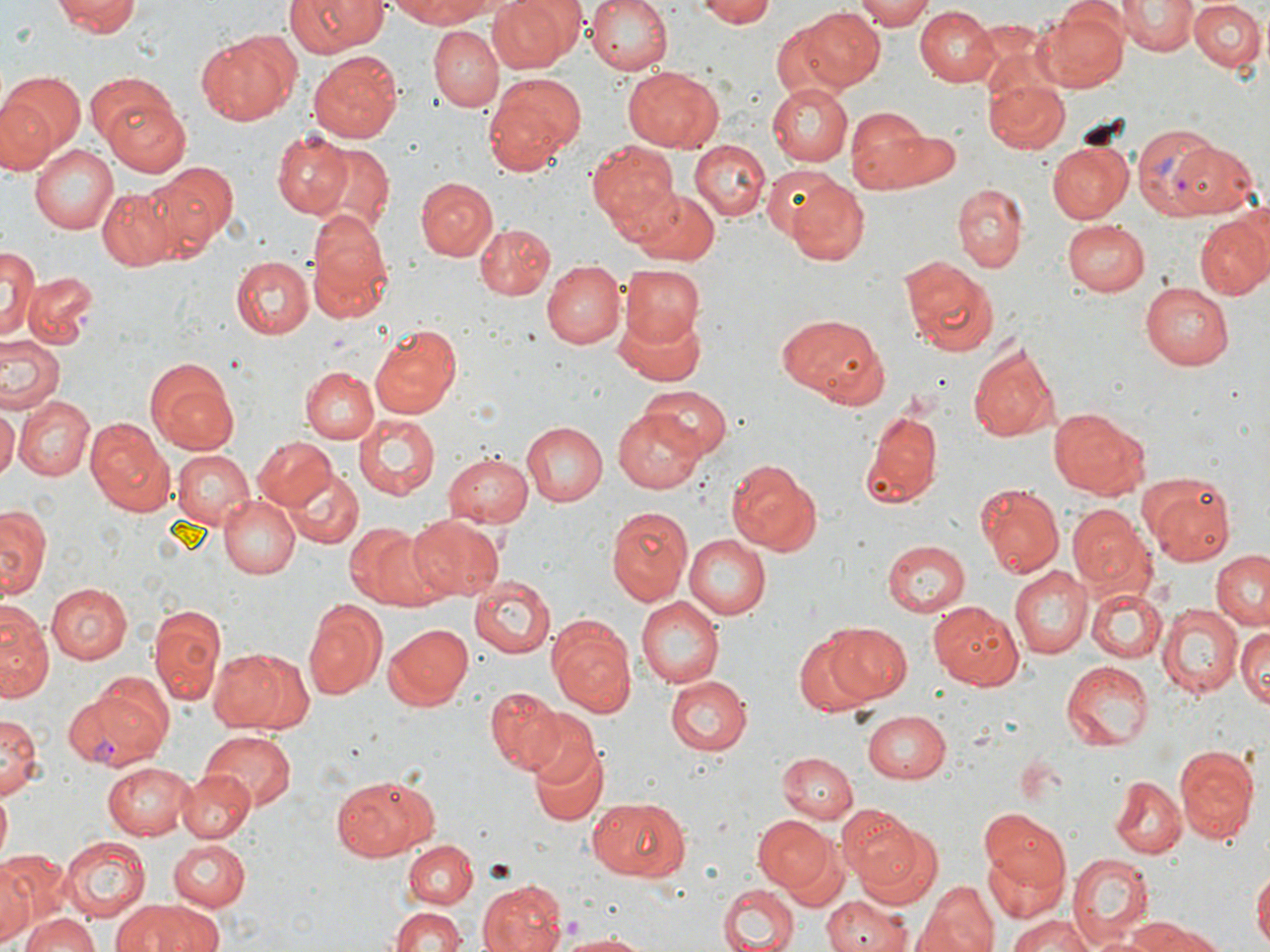
Summary:
  - Coordinate format: approximate bounding boxes as (x1,y1)-(x2,y2) corner pairs in pixels
  - Plasmodium vivax-infected red blood cell locations: (1130,124)-(1223,218), (66,679)-(171,768)
  - Uninfected red blood cell locations: (50,0)-(141,38), (284,0)-(389,58), (583,0)-(673,75), (855,0)-(938,29), (1119,0)-(1194,55), (387,1)-(497,28), (488,1)-(571,72), (697,1)-(780,27), (1190,1)-(1267,74), (1041,5)-(1130,89), (915,6)-(1001,85), (800,8)-(884,91), (769,21)-(849,99), (428,26)-(504,110), (194,30)-(300,126), (308,51)-(404,143), (623,66)-(723,152), (2,70)-(85,160), (482,73)-(585,175), (984,76)-(1070,156), (768,84)-(852,166), (97,86)-(191,173), (0,95)-(57,173), (845,106)-(932,192), (875,123)-(961,189), (270,128)-(352,217), (691,139)-(771,223), (585,140)-(679,228), (1048,141)-(1134,223), (28,142)-(118,235), (316,142)-(394,234), (1168,144)-(1259,217), (148,163)-(238,251), (761,164)-(841,241), (415,177)-(498,261), (785,178)-(869,265), (96,184)-(185,271), (954,185)-(1027,271), (630,189)-(720,265), (306,212)-(396,323), (1194,214)-(1269,299), (1061,219)-(1151,297), (474,223)-(557,299), (1,247)-(40,337), (231,255)-(314,340), (900,257)-(999,359), (543,261)-(624,349), (618,264)-(706,350), (23,270)-(99,348), (1141,280)-(1234,371), (611,306)-(710,387), (778,311)-(886,406), (369,324)-(461,418), (0,335)-(66,415), (968,339)-(1059,443), (300,365)-(379,443), (148,366)-(240,455), (639,385)-(732,458), (13,396)-(95,481), (0,404)-(18,481), (614,407)-(705,491), (1049,407)-(1150,499), (355,412)-(443,497), (860,412)-(942,511), (520,421)-(606,506), (87,425)-(176,517), (253,436)-(336,511), (170,449)-(255,530), (443,450)-(532,529), (725,461)-(822,554), (289,470)-(363,547), (1139,475)-(1239,565), (977,486)-(1064,579), (217,494)-(300,579), (0,504)-(49,601), (606,505)-(694,604), (1066,505)-(1155,594), (408,515)-(505,600), (344,525)-(429,608), (681,533)-(770,623), (881,540)-(971,615), (1210,550)-(1269,631), (1011,567)-(1090,658), (468,577)-(556,658), (48,584)-(132,665), (1085,588)-(1166,664), (636,597)-(724,688), (303,598)-(386,701), (930,600)-(1026,689), (1,603)-(52,702), (1158,603)-(1242,695), (149,604)-(226,706), (819,616)-(1009,699), (548,620)-(636,717), (1235,620)-(1270,710), (822,622)-(913,703), (385,624)-(473,710), (795,634)-(871,716), (209,645)-(308,734), (1062,660)-(1155,752), (664,676)-(749,754), (485,688)-(567,774), (863,710)-(953,784), (526,711)-(603,792), (0,714)-(40,801), (200,731)-(295,813), (526,740)-(607,829), (1174,747)-(1257,838), (776,752)-(858,822), (104,763)-(194,838), (176,769)-(255,843), (335,775)-(435,861), (1109,777)-(1186,858), (587,797)-(690,882), (838,807)-(925,889), (979,811)-(1072,895), (755,816)-(834,892), (861,825)-(944,909), (60,837)-(147,920), (167,840)-(251,911), (402,840)-(476,911), (781,846)-(848,912), (984,847)-(1063,927), (1065,851)-(1156,948), (2,866)-(41,943), (1253,867)-(1270,952), (6,871)-(83,951), (916,879)-(1000,952), (478,880)-(566,952), (717,882)-(798,952), (822,896)-(910,952), (113,899)-(219,952), (391,906)-(466,952), (18,911)-(100,952), (1006,915)-(1095,952), (1120,916)-(1216,952), (560,930)-(653,950)
  - Slide-level diagnosis: Plasmodium vivax
  - Magnification: 1000x
  - Image size: 1270×952 pixels
  - Preparation: thin blood smear
  - Stain: May-Grünwald-Giemsa
  - Modality: light microscopy
  - Field of view: single